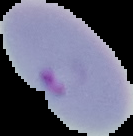
Summary:
  - Image type: cell region segmented out of the field of view; surrounding area masked to black
  - Preparation: thin blood film
  - Image size: 133×136 pixels
  - Malaria status: parasitized